State the preparation type.
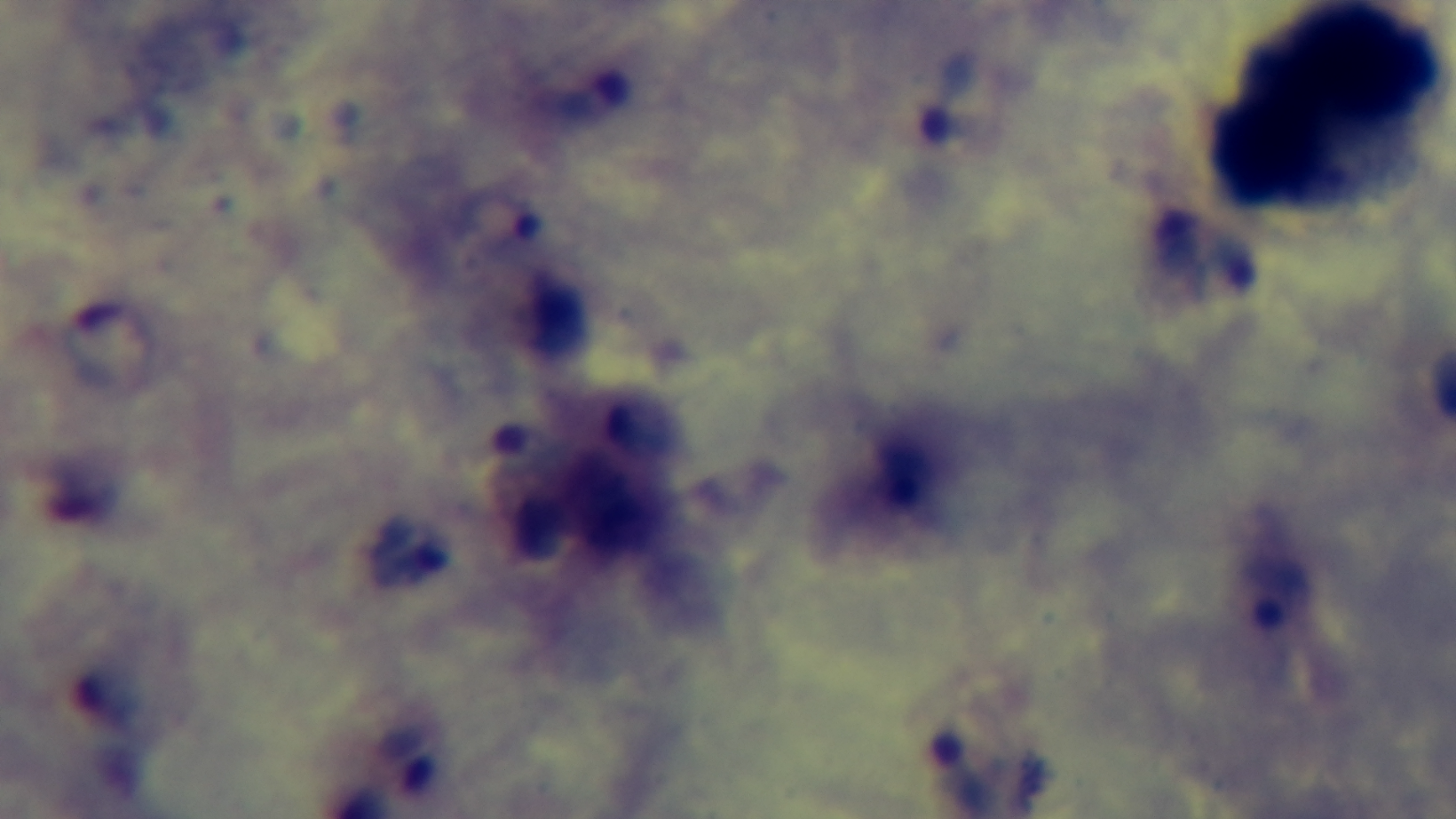

It is a thick blood film.

Summary:
  - Malaria status: positive
  - Objective: 100x oil immersion
  - Stain: Giemsa
  - Capture: mounted 4K digital camera
  - Field of view: single
  - Modality: light microscopy